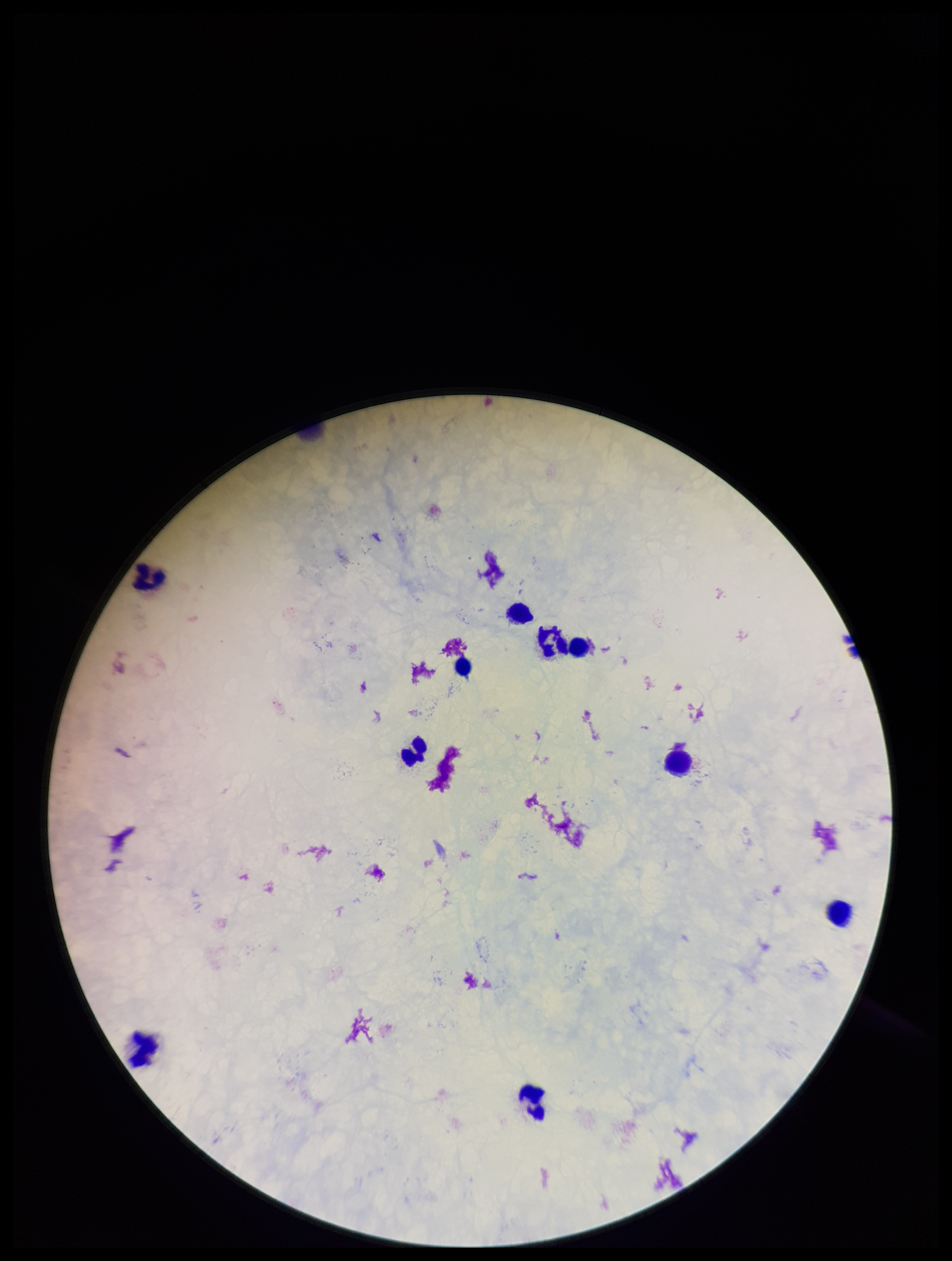
Single field of view. Giemsa stain. Leukocyte count: 10. Preparation: thick. Parasite count: 0. Plasmodium parasites: none seen. Smartphone photograph taken through the eyepiece of a microscope. Patient malaria status: negative. Image is 952×1261 pixels.